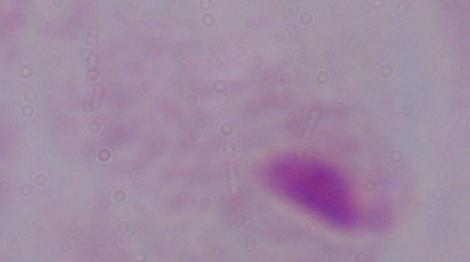 Micrograph. 1000x magnification. A trichomonad is shown.